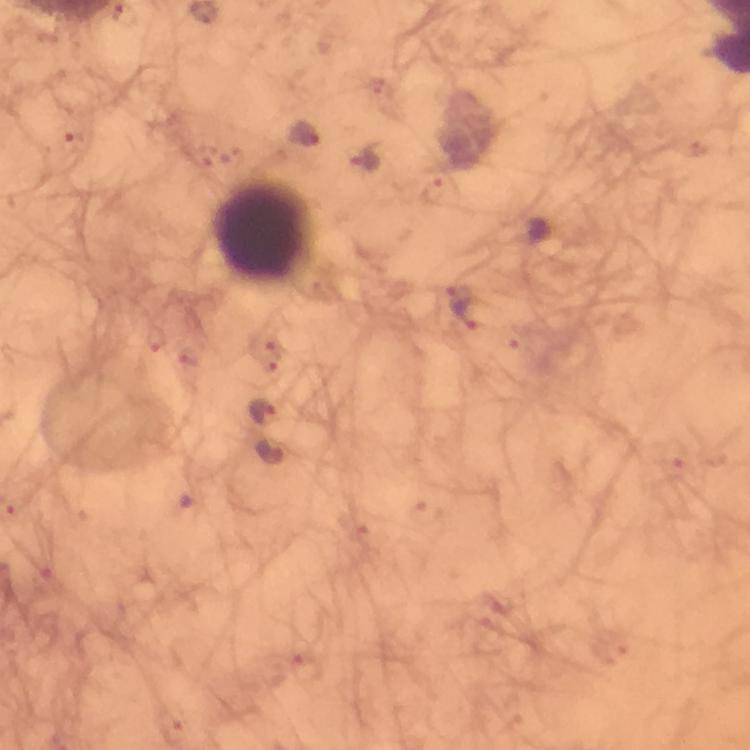
cropped from = one field of view
image size = 750×750 pixels
capture = smartphone photograph through a microscope
context = from a malaria diagnostic workup
stain = Giemsa
leukocyte locations = approximate object centers, in pixels from the top-left corner: (x=264, y=230)
preparation = thick blood film
Plasmodium parasite locations = approximate object centers, in pixels from the top-left corner: (x=263, y=409)
magnification = 100x
immersion oil = used